Assess the morphology of the erythrocytes.
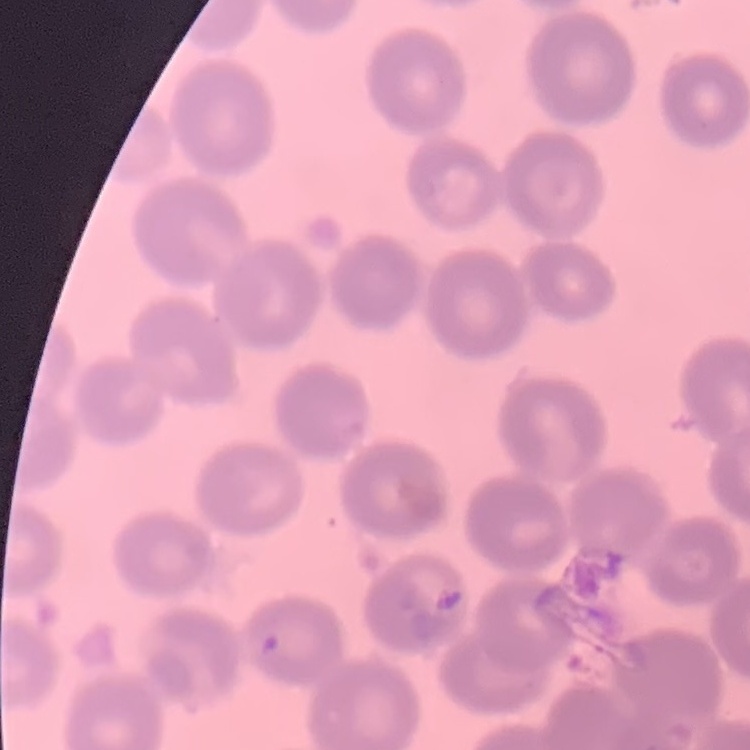

They show no rouleaux formation.

Summary:
  - Preparation: thin blood smear
  - Stain: Field's or Giemsa
  - Image type: square crop of a larger photomicrograph